Report the malaria status of this cell.
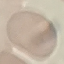
It is uninfected.

Summary:
  - Image type: automatically extracted cell patch, resized to 64 × 64 pixels
  - Stain: Giemsa
  - Preparation: thin blood film
  - Capture: smartphone camera at the microscope eyepiece